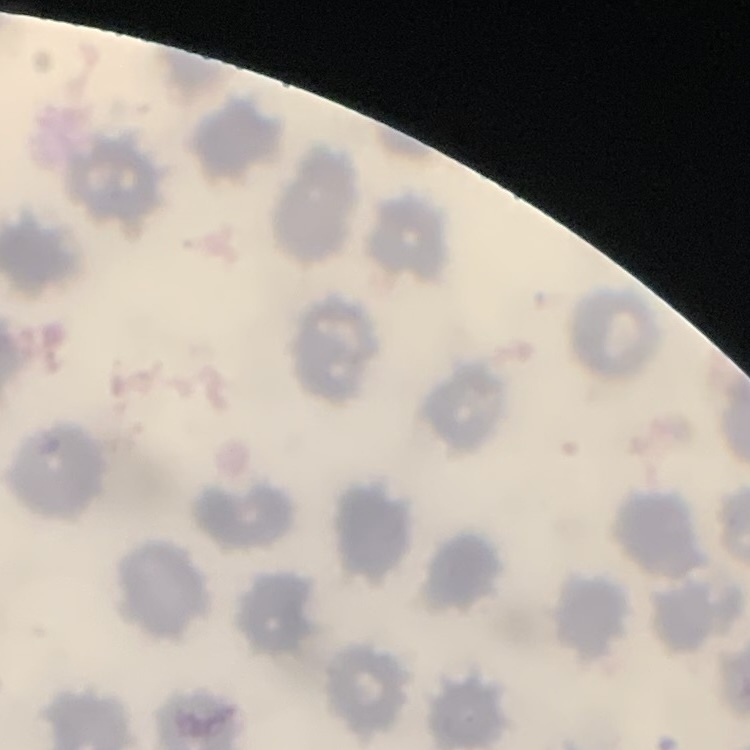
erythrocyte_morphology: no rouleaux formation
image_type: square crop of a larger photomicrograph
preparation: thin peripheral smear
stain: Field's or Giemsa